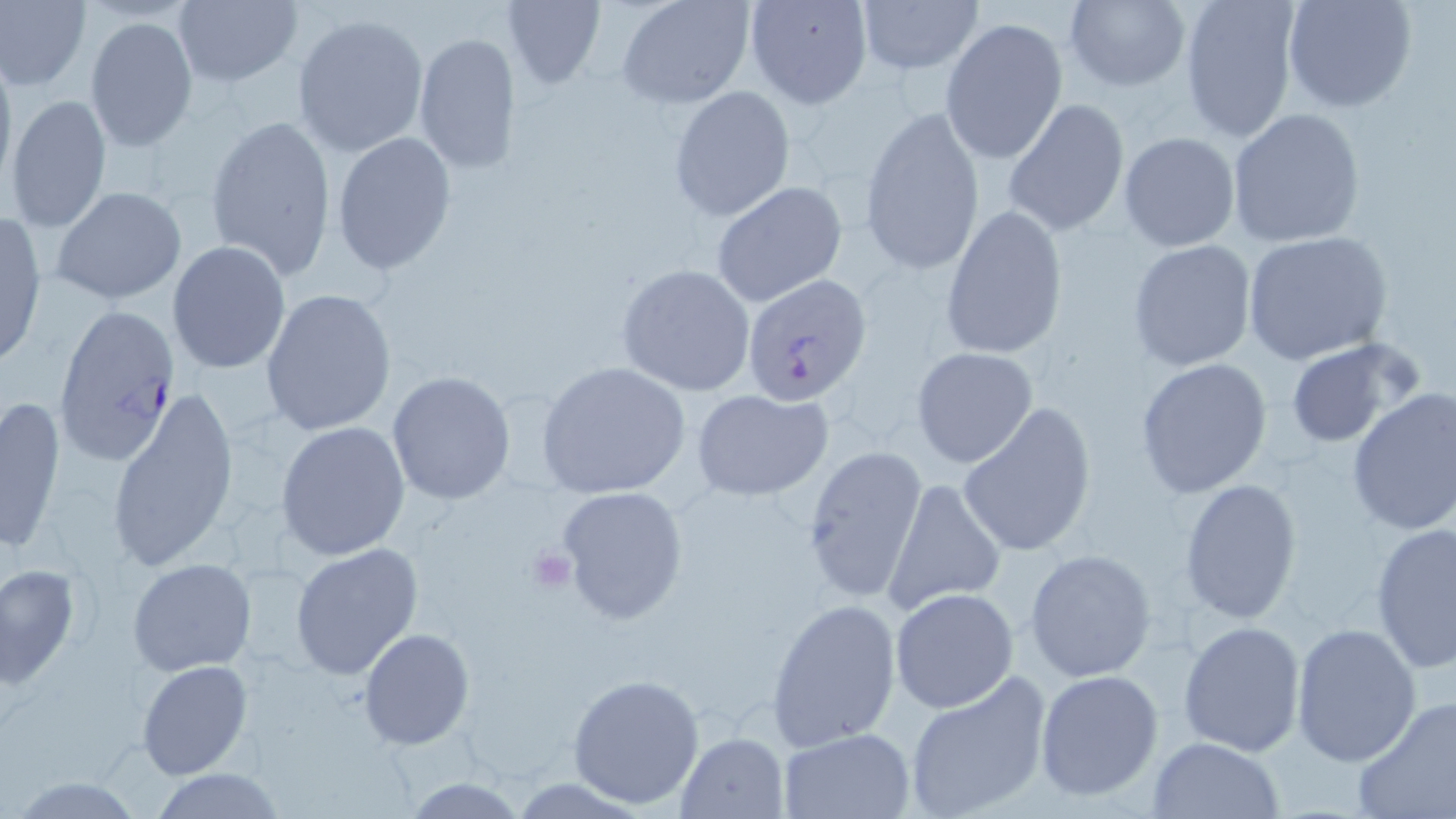 Approximate bounding boxes as (x1, y1, x2, y2) in pixels. Plasmodium falciparum-infected red blood cell locations: (741, 272, 874, 404), (52, 302, 183, 465). Platelet locations: (527, 548, 577, 595). Uninfected red blood cell locations: (0, 0, 90, 92), (171, 0, 302, 88), (502, 0, 606, 88), (616, 0, 754, 108), (742, 0, 874, 110), (854, 0, 984, 78), (1060, 0, 1189, 93), (1178, 0, 1302, 144), (1282, 0, 1418, 115), (291, 12, 429, 158), (84, 16, 198, 154), (940, 17, 1069, 165), (413, 32, 522, 176), (0, 48, 17, 193), (668, 87, 795, 221), (5, 93, 113, 235), (1003, 98, 1131, 236), (858, 104, 985, 277), (1226, 108, 1367, 248), (205, 113, 337, 280), (1119, 131, 1240, 251), (331, 133, 456, 275), (711, 181, 847, 308), (50, 187, 188, 303), (940, 205, 1066, 357), (0, 214, 49, 370), (1241, 230, 1394, 366), (1126, 238, 1257, 372), (167, 240, 290, 374), (614, 264, 756, 396), (261, 288, 398, 439), (1283, 337, 1419, 451), (910, 346, 1039, 467), (1134, 357, 1275, 499), (536, 362, 691, 500), (387, 371, 516, 506), (105, 382, 240, 580), (688, 387, 836, 502), (1346, 387, 1456, 535), (1, 395, 67, 552), (957, 400, 1097, 557), (277, 421, 411, 560), (800, 446, 922, 601), (882, 477, 1006, 613), (1178, 477, 1303, 624), (555, 484, 690, 626), (1369, 521, 1455, 673), (290, 544, 423, 681), (1025, 549, 1158, 684), (127, 557, 258, 676), (1, 561, 82, 690), (890, 588, 1019, 713), (766, 597, 902, 749), (1178, 620, 1307, 758), (1291, 621, 1423, 767), (358, 628, 474, 749), (136, 659, 252, 780), (1034, 668, 1164, 800), (568, 673, 705, 809), (901, 675, 1051, 819), (1353, 695, 1456, 819), (778, 727, 915, 818), (673, 732, 790, 819), (1147, 737, 1285, 819), (148, 768, 289, 819), (6, 776, 151, 817), (402, 777, 527, 817). Slide-level diagnosis: Plasmodium falciparum. May-Grünwald-Giemsa-stained preparation. Thin blood film. Image is 1456×819 pixels. Light microscopy. Single field of view. 1000x magnification.